Assess this cell for malaria.
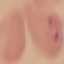

Uninfected.

Acquired by smartphone through the microscope eyepiece. Thin blood film. Automatically extracted cell patch, resized to 64 × 64 pixels. Giemsa stain.